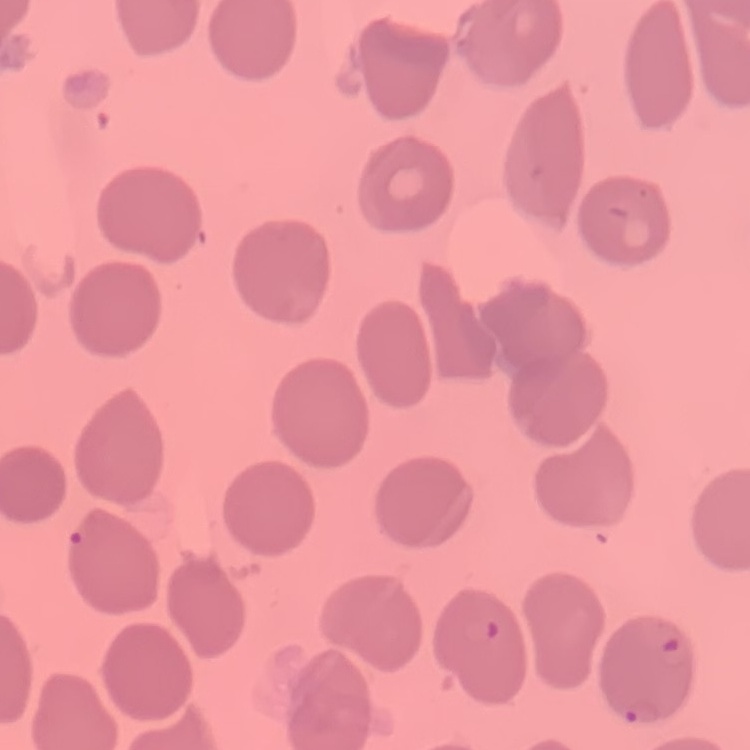
Summary:
  - Red blood cell morphology: no rouleaux formation
  - Preparation: thin peripheral smear
  - Image type: one tile cut from a larger photomicrograph
  - Stain: Field's or Giemsa